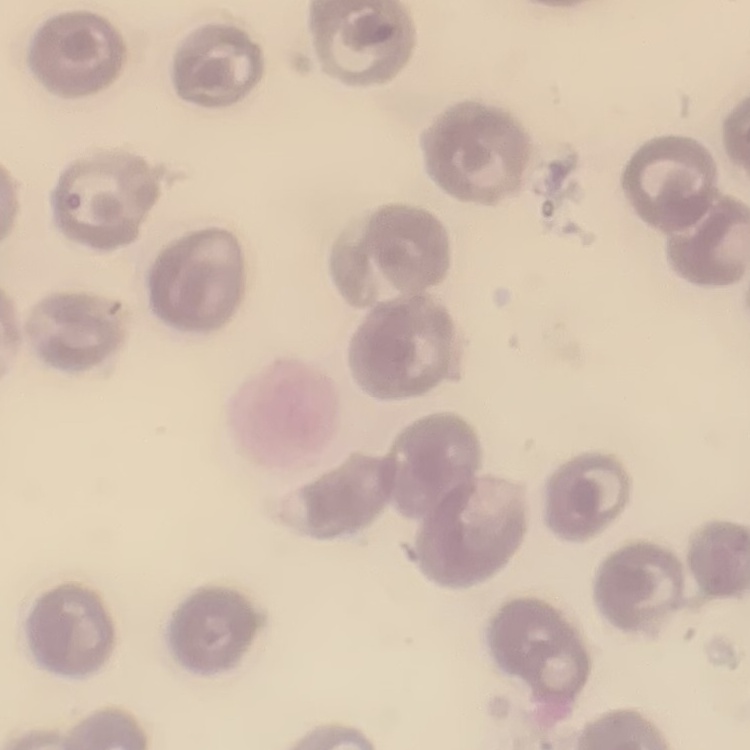
The erythrocytes exhibit no rouleaux formation. One tile cut from a larger photomicrograph. Field's or Giemsa stain. Thin blood smear.